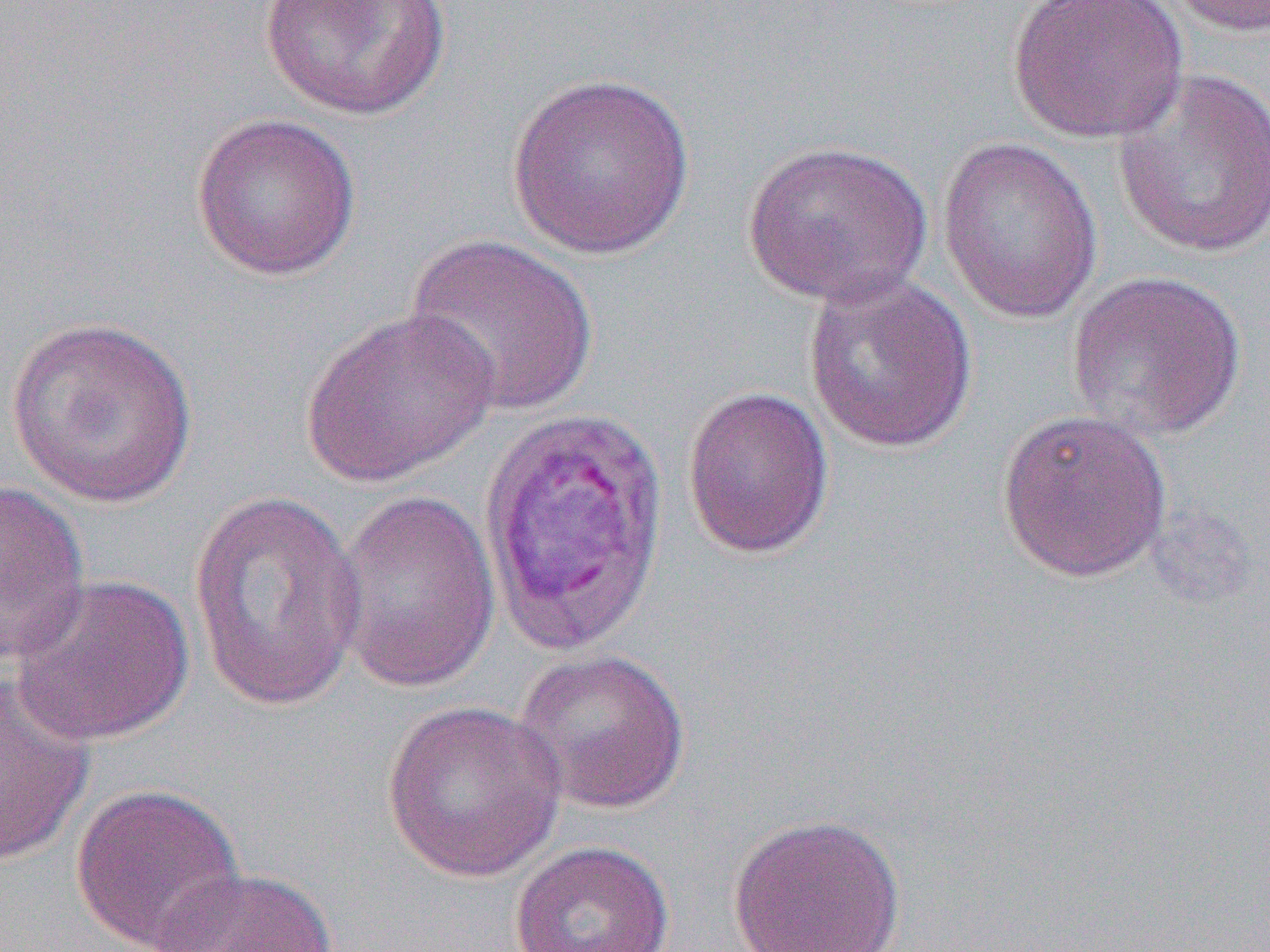 Approximate bounding boxes as (x1,y1)-(x2,y2) corner pairs in pixels. Uninfected red blood cell locations: (258,0)-(453,121), (1008,0)-(1190,144), (1164,0)-(1270,38), (1111,68)-(1270,261), (506,71)-(697,260), (190,112)-(361,282), (937,135)-(1103,325), (741,138)-(933,309), (403,234)-(599,418), (802,270)-(978,454), (1065,270)-(1247,442), (301,306)-(501,488), (5,316)-(199,509), (682,385)-(834,558), (996,408)-(1173,583), (0,479)-(92,665), (331,488)-(502,696), (188,489)-(367,712), (11,573)-(194,747), (512,648)-(692,814), (0,679)-(95,867), (380,699)-(568,883), (70,782)-(246,952), (727,813)-(906,952), (509,840)-(675,952), (157,867)-(335,952). Slide-level diagnosis: Plasmodium vivax. 1000x magnification. Thin blood film. One field of a larger specimen. Optical microscopy. Image is 1270×952 pixels.